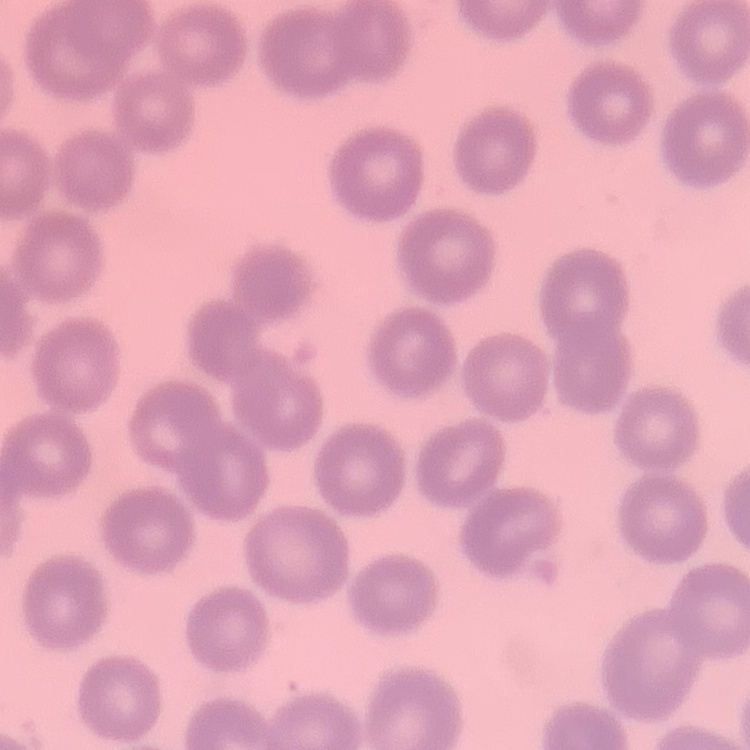
erythrocyte morphology = no rouleaux formation
stain = Field's or Giemsa
preparation = thin blood film
image type = one tile cut from a larger photomicrograph